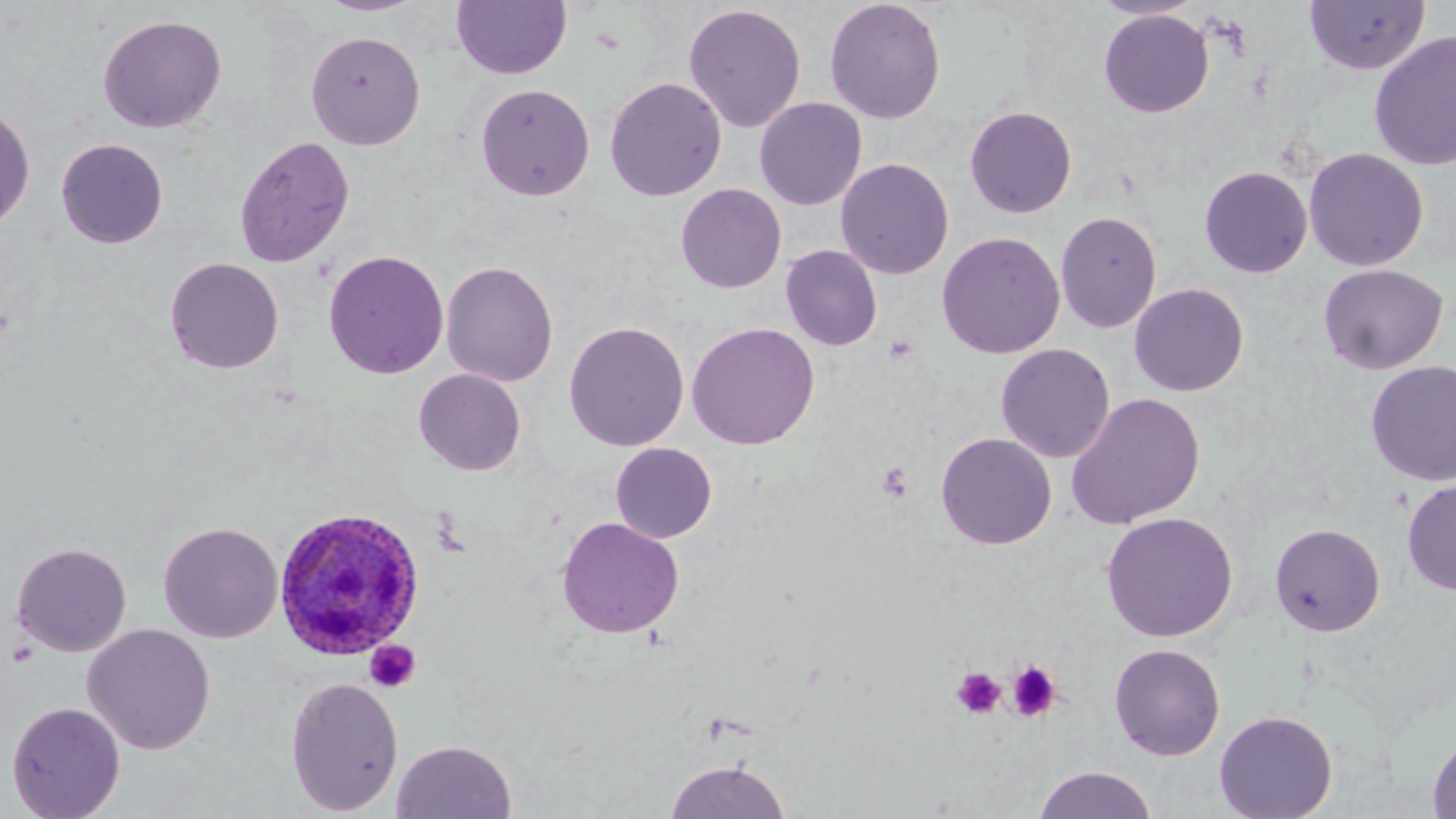
Approximate bounding boxes as [x1, y1, x2, y2] in pixels. Uninfected red blood cell locations: [314, 0, 428, 17], [451, 0, 571, 80], [824, 0, 947, 125], [1091, 0, 1205, 20], [1304, 1, 1429, 75], [683, 3, 806, 133], [1098, 9, 1215, 118], [97, 14, 227, 134], [306, 29, 426, 149], [1368, 30, 1456, 172], [604, 77, 726, 201], [475, 83, 595, 201], [754, 97, 867, 210], [0, 103, 35, 231], [964, 105, 1078, 218], [234, 135, 355, 267], [56, 138, 169, 248], [1303, 147, 1428, 271], [835, 157, 954, 280], [1199, 166, 1313, 278], [676, 183, 787, 293], [1055, 210, 1162, 333], [936, 231, 1065, 360], [781, 245, 883, 351], [323, 249, 449, 379], [164, 257, 284, 374], [441, 260, 559, 386], [1317, 263, 1449, 375], [1129, 282, 1249, 397], [563, 321, 689, 452], [686, 322, 820, 450], [995, 343, 1115, 463], [1365, 360, 1456, 486], [413, 368, 527, 476], [1065, 392, 1206, 530], [935, 432, 1057, 550], [610, 442, 717, 543], [1402, 478, 1456, 595], [1100, 511, 1238, 642], [556, 516, 685, 639], [158, 521, 283, 643], [1270, 522, 1385, 636], [11, 542, 132, 657], [81, 623, 216, 755], [1109, 643, 1226, 761], [284, 676, 404, 815], [6, 701, 126, 818], [1214, 710, 1338, 819], [1426, 732, 1456, 819], [391, 739, 517, 819], [665, 758, 791, 819], [1033, 766, 1158, 819]. Plasmodium ovale-infected red blood cell locations: [272, 507, 425, 661]. Platelet locations: [876, 462, 913, 502], [364, 639, 421, 694], [1007, 661, 1063, 722], [951, 667, 1006, 719]. Slide-level diagnosis: Plasmodium ovale. May-Grünwald-Giemsa-stained preparation. Light microscopy. 1000x magnification. Image is 1456×819 pixels. Thin blood film. Single field of view.